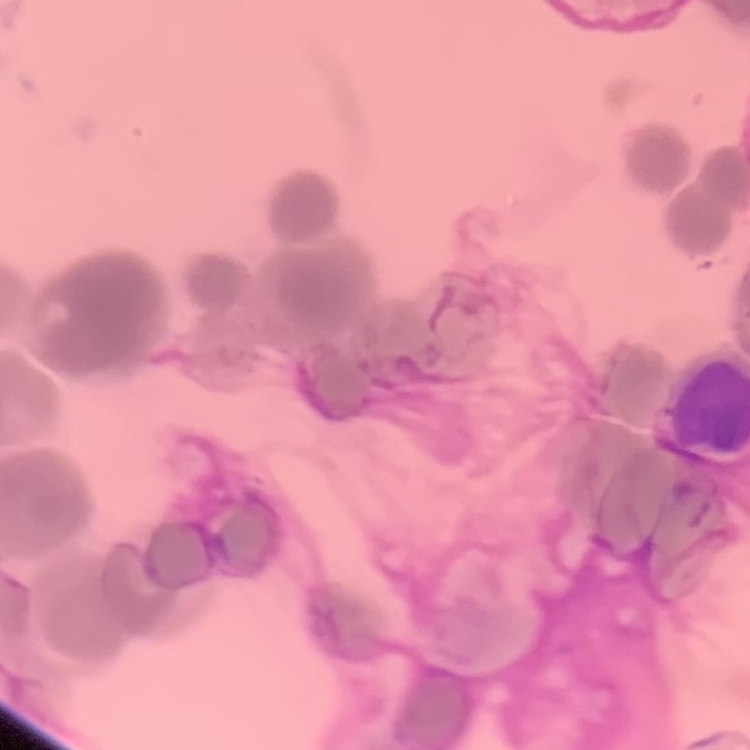

erythrocyte morphology = rouleaux formation
preparation = thin peripheral smear
image type = square crop of a larger photomicrograph
stain = Field's or Giemsa